Identify the parasite.
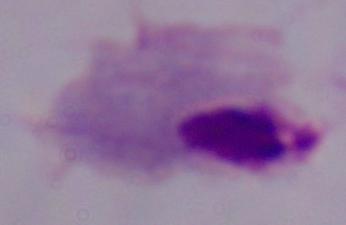

A trichomonad.

{
  "modality": "photomicrograph",
  "magnification": "1000x"
}